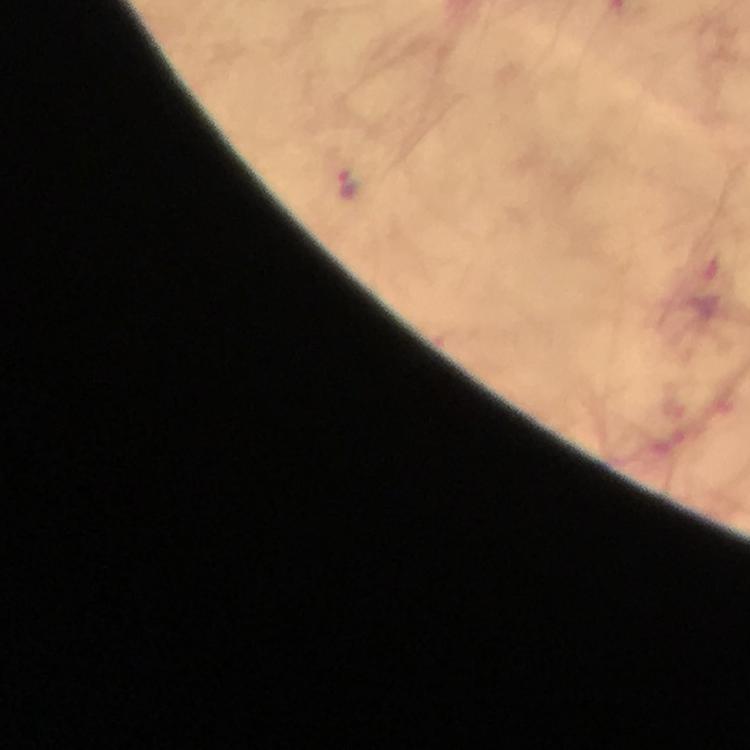

magnification = 100x
cropped from = one field of view
context = from a malaria diagnostic workup
image size = 750×750 pixels
malaria parasite locations = approximate centers as {x, y} in pixels: {348, 182}
preparation = thick smear
capture = smartphone camera through the microscope
stain = Giemsa
immersion oil = applied